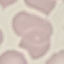

Result: negative for malaria parasites. Acquired by smartphone through the microscope eyepiece. Automatically extracted cell patch, resized to 64 × 64 pixels. Giemsa-stained preparation. Thin smear of blood.